Locate every malaria parasite.
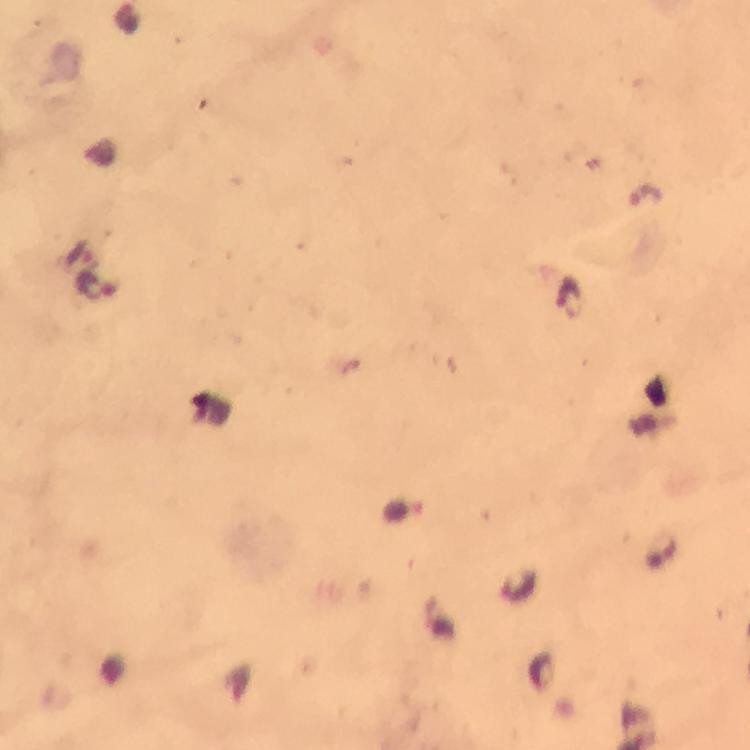
Approximate centers as [x, y] in pixels.
Malaria parasites: [97, 286], [569, 295].

Summary:
  - Stain: Giemsa
  - Immersion oil: applied
  - Capture: smartphone mounted on the microscope
  - Magnification: 100x
  - Image size: 750×750 pixels
  - Cropped from: a single field of view
  - Context: from a diagnostic examination for malaria
  - Preparation: thick smear